Report the malaria status of this cell.
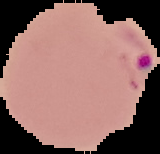

Parasitized.

Summary:
  - Preparation: thin blood smear
  - Image size: 160×154 pixels
  - Image type: segmented cell region with the area outside set to black